Classify this cell by malaria status.
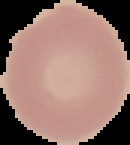
Uninfected.

image_size: 130×145 pixels
preparation: thin blood smear
image_type: segmented cell region with the area outside set to black